Name the blood parasite species.
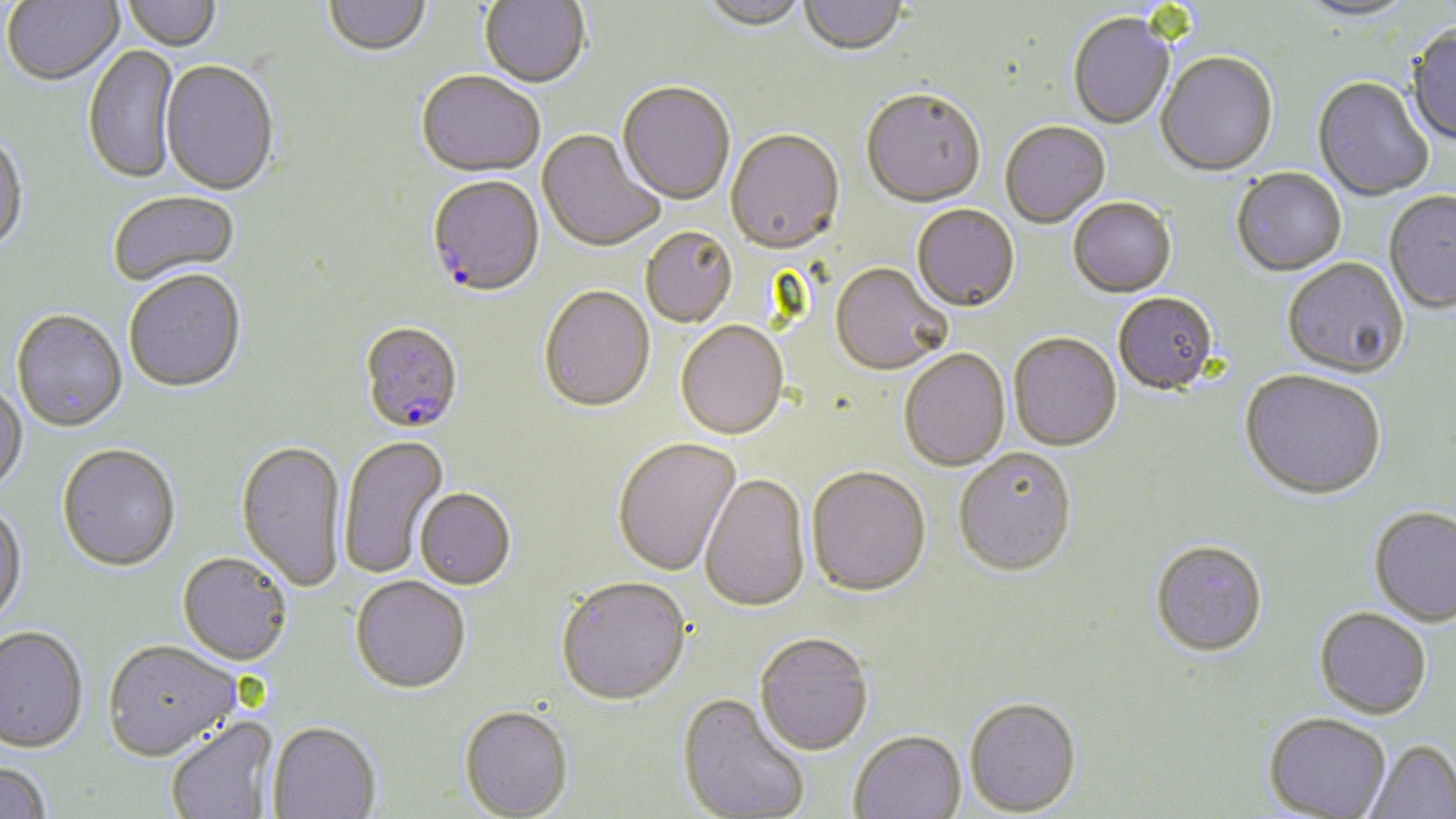
Plasmodium falciparum.

Approximate bounding boxes as (x1,y1)-(x2,y2) corner pairs in pixels. Plasmodium falciparum-infected red blood cell locations: (426,177)-(545,300), (358,324)-(463,435). Uninfected red blood cell locations: (3,0)-(124,88), (122,0)-(221,53), (480,0)-(590,90), (699,0)-(808,34), (1294,0)-(1419,24), (324,1)-(430,58), (799,1)-(907,58), (1068,15)-(1175,130), (1406,25)-(1456,148), (83,46)-(180,185), (1155,54)-(1278,178), (160,62)-(279,199), (416,73)-(544,180), (1312,78)-(1433,202), (617,83)-(735,207), (861,91)-(985,210), (1000,123)-(1111,229), (537,130)-(665,254), (725,131)-(845,257), (0,133)-(29,255), (1231,169)-(1346,278), (107,191)-(241,289), (1384,192)-(1456,316), (1068,199)-(1177,299), (912,205)-(1019,314), (641,228)-(737,329), (1282,259)-(1409,381), (830,265)-(952,377), (123,271)-(247,394), (538,288)-(655,415), (1113,294)-(1218,397), (11,309)-(128,434), (675,323)-(788,442), (1009,334)-(1122,453), (899,350)-(1010,473), (1240,372)-(1386,503), (0,380)-(28,495), (338,435)-(450,579), (235,439)-(347,592), (612,439)-(742,578), (57,443)-(181,571), (953,451)-(1077,579), (806,469)-(932,600), (699,475)-(810,615), (414,488)-(517,591), (0,502)-(27,628), (1368,509)-(1456,629), (1149,543)-(1267,660), (177,551)-(293,665), (350,576)-(471,694), (555,579)-(691,708), (1313,610)-(1431,722), (0,625)-(89,752), (754,634)-(874,757), (103,638)-(241,759), (676,693)-(810,818), (964,698)-(1082,817), (458,705)-(573,818), (165,716)-(280,819), (1263,716)-(1390,818), (268,720)-(381,818), (849,731)-(965,819), (1367,742)-(1456,819), (0,759)-(52,818). 1000x magnification. Image is 1456×819 pixels. Thin blood film. May-Grünwald-Giemsa-stained preparation. Optical microscopy. One field of a larger specimen.